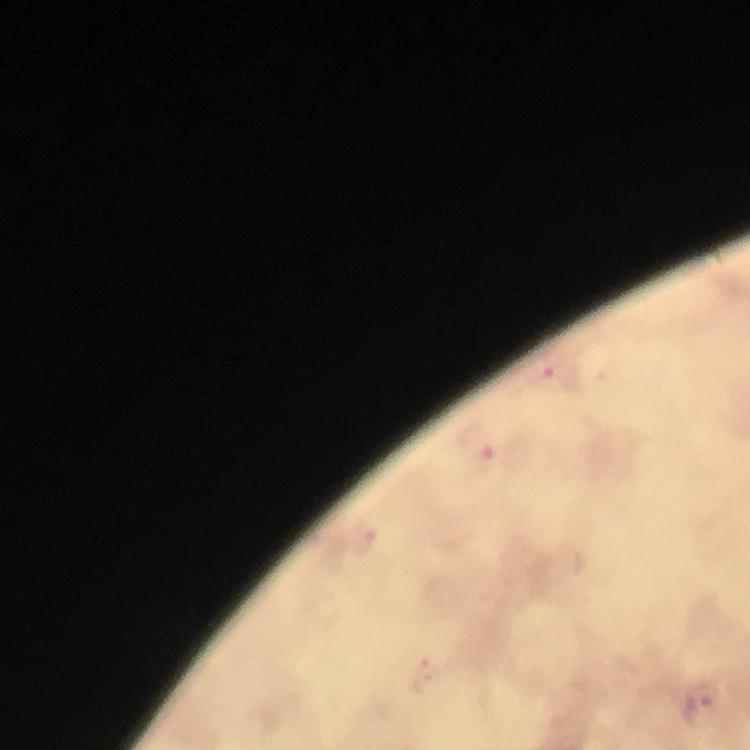
Approximate centers as {x, y} in pixels.
Summary:
  - Malaria parasite locations: {548, 376}, {483, 461}, {364, 541}, {426, 676}, {703, 697}
  - Magnification: 100x
  - Stain: Giemsa
  - Context: from a diagnostic examination for malaria
  - Immersion oil: applied
  - Preparation: thick blood smear
  - Capture: smartphone photograph through a microscope
  - Cropped from: a single field of view
  - Image size: 750×750 pixels